Locate every Plasmodium parasite.
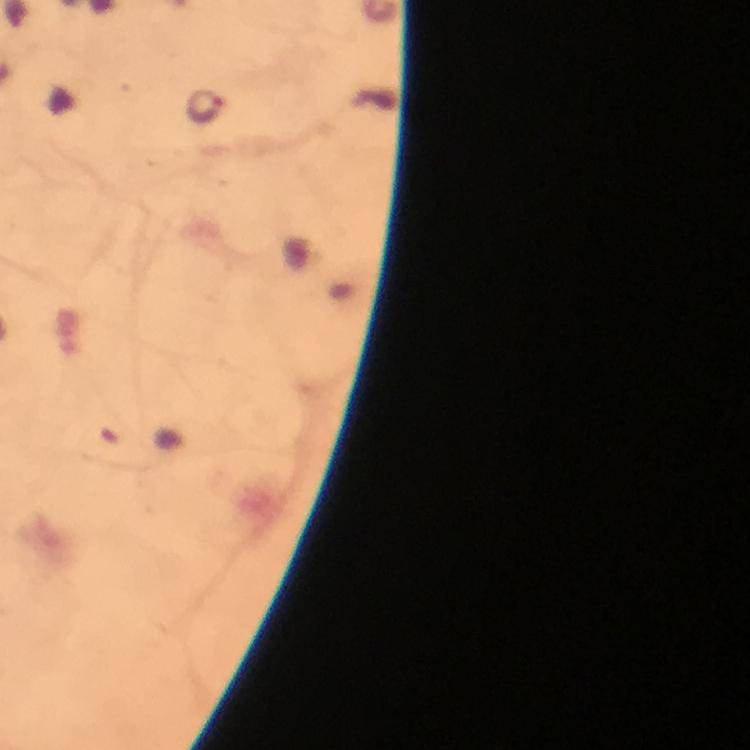

Approximate centers as [x, y] in pixels.
Plasmodium parasites: [205, 106].

preparation: thick blood smear
immersion_oil: applied
context: from a diagnostic examination for malaria
image_size: 750×750 pixels
cropped_from: one field of view
magnification: 100x
capture: smartphone mounted on the microscope
stain: Giemsa